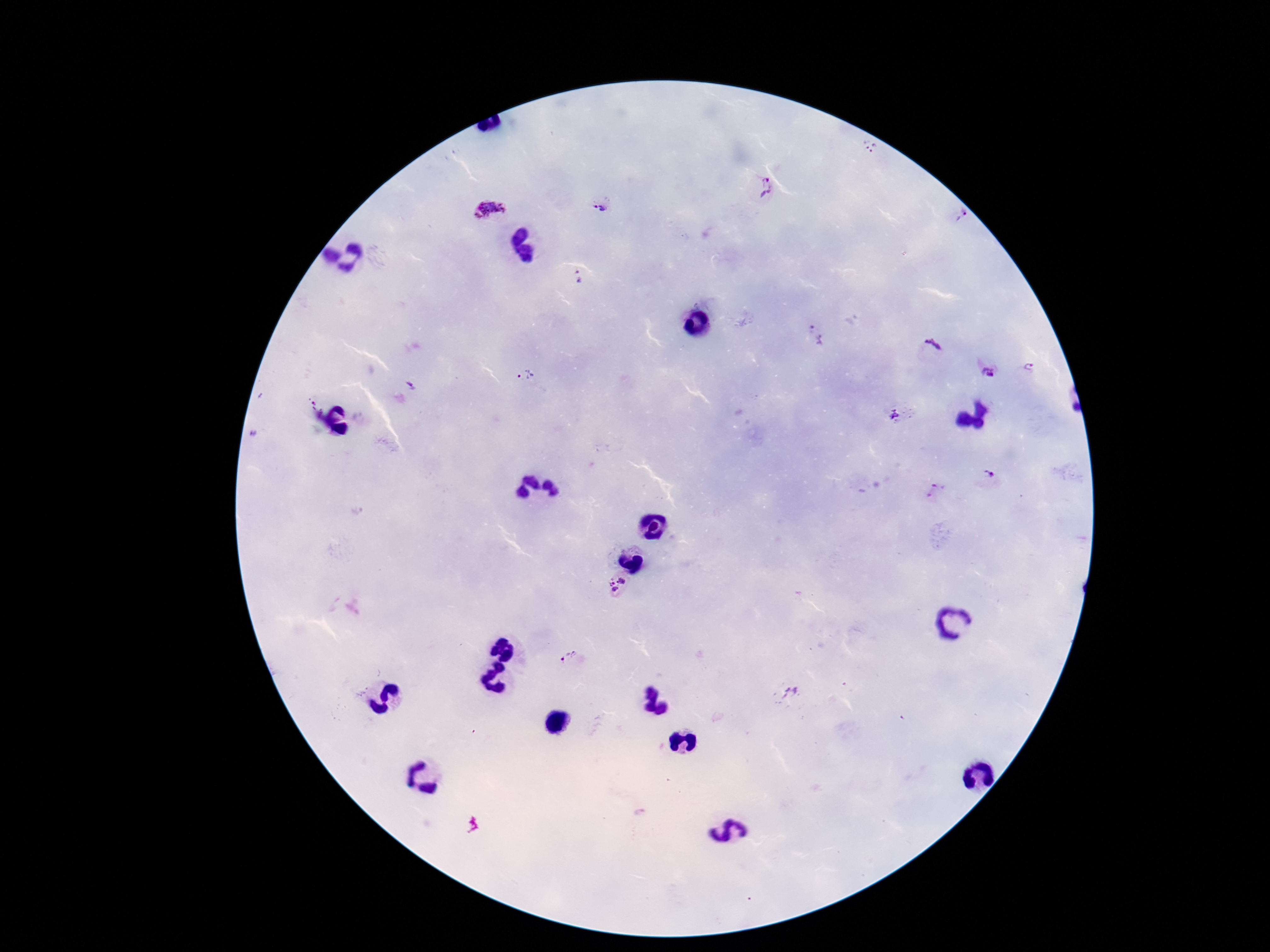
{
  "capture": "smartphone camera through the microscope eyepiece",
  "magnification": "100x",
  "image_size": "1270×952 pixels",
  "preparation": "thick peripheral-blood smear",
  "patient_malaria_status": "infected",
  "stain": "Giemsa",
  "plasmodium_parasite_locations": "approximate object centers, in pixels from the top-left corner: (x=869, y=146), (x=765, y=186), (x=600, y=207), (x=491, y=212), (x=961, y=215), (x=578, y=277), (x=815, y=335), (x=933, y=347), (x=1028, y=368), (x=986, y=371), (x=524, y=377), (x=893, y=415), (x=988, y=476), (x=933, y=491), (x=621, y=581), (x=610, y=582), (x=616, y=590), (x=568, y=658), (x=788, y=694)",
  "field_of_view": "single"
}